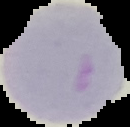

image size = 130×127 pixels
preparation = thin blood film
image type = segmented cell region on a black background
result = negative for Plasmodium parasites